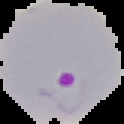
Summary:
  - Image size: 124×124 pixels
  - Result: Plasmodium parasites identified
  - Image type: cell region segmented out of the field of view; surrounding area masked to black
  - Preparation: thin blood smear